Locate every blood parasite and identify its species.
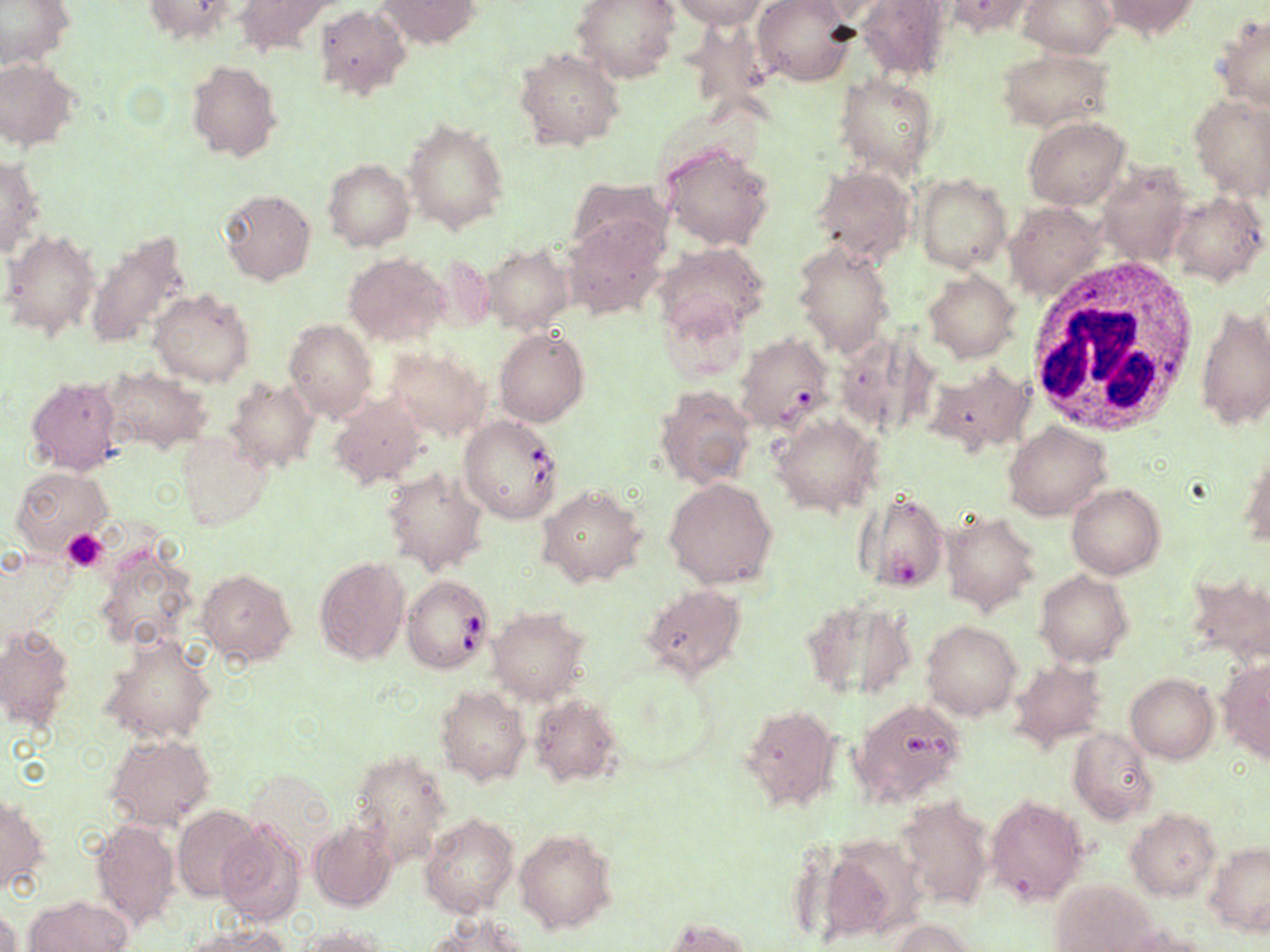

Approximate bounding boxes as (x1, y1, x2, y2) in pixels.
Babesia divergens-infected red blood cells: (733, 339, 831, 431), (459, 415, 564, 523), (403, 575, 494, 675).
No Plasmodium falciparum, Plasmodium ovale, Plasmodium malariae, Plasmodium vivax, or Trypanosoma brucei observed.

Platelet locations: (60, 528, 109, 574). Uninfected red blood cell locations: (0, 0, 73, 67), (142, 0, 240, 45), (232, 0, 340, 54), (376, 0, 479, 48), (572, 0, 681, 83), (671, 0, 770, 28), (755, 0, 858, 87), (1018, 0, 1116, 58), (856, 1, 952, 82), (940, 1, 1044, 39), (1100, 1, 1200, 40), (314, 4, 410, 100), (1217, 14, 1270, 110), (516, 49, 623, 150), (996, 49, 1114, 130), (0, 58, 81, 150), (186, 59, 280, 162), (835, 72, 939, 180), (1190, 93, 1270, 199), (1024, 116, 1129, 209), (403, 118, 508, 234), (659, 142, 776, 251), (0, 154, 44, 260), (323, 158, 415, 251), (1099, 164, 1192, 267), (812, 165, 916, 265), (914, 174, 1011, 273), (566, 177, 672, 257), (219, 189, 316, 286), (1167, 190, 1267, 285), (1005, 202, 1105, 299), (561, 217, 667, 319), (84, 228, 194, 349), (3, 229, 101, 338), (654, 242, 771, 339), (792, 242, 895, 356), (484, 245, 573, 333), (345, 253, 447, 344), (429, 254, 495, 332), (924, 269, 1020, 361), (150, 288, 254, 387), (656, 296, 752, 386), (1196, 303, 1269, 432), (283, 319, 377, 422), (484, 325, 581, 518), (496, 329, 589, 426), (385, 346, 490, 441), (926, 364, 1033, 457), (100, 367, 212, 454), (25, 376, 123, 475), (226, 376, 318, 472), (656, 384, 756, 489), (330, 392, 428, 490), (773, 415, 879, 515), (1003, 422, 1111, 519), (175, 431, 269, 530), (1240, 448, 1269, 547), (11, 466, 112, 553), (383, 467, 485, 575), (664, 477, 778, 590), (1067, 485, 1164, 579), (539, 486, 646, 586), (855, 491, 944, 595), (941, 511, 1041, 615), (92, 541, 201, 656), (313, 555, 409, 666), (197, 568, 296, 664), (1189, 569, 1270, 664), (1036, 571, 1133, 666), (640, 586, 745, 681), (803, 595, 914, 701), (488, 608, 588, 704), (923, 621, 1021, 719), (0, 623, 76, 732), (100, 637, 217, 745), (1009, 658, 1109, 749), (1221, 659, 1270, 761), (1127, 674, 1217, 763), (436, 686, 529, 786), (528, 693, 623, 787), (737, 705, 841, 811), (849, 708, 969, 805), (1068, 727, 1159, 823), (106, 733, 215, 832), (347, 748, 452, 864), (987, 794, 1088, 905), (1, 796, 45, 896), (896, 796, 993, 908), (174, 806, 260, 901), (1127, 808, 1219, 900), (420, 813, 519, 918), (215, 817, 306, 926), (92, 819, 180, 931), (309, 820, 398, 911), (514, 829, 618, 933), (819, 834, 925, 943), (1205, 842, 1269, 936), (1049, 882, 1153, 951), (28, 895, 130, 951), (0, 907, 20, 952), (424, 915, 533, 952), (661, 917, 751, 952), (889, 918, 979, 952), (185, 923, 293, 952), (297, 924, 394, 951), (1115, 926, 1218, 952). White blood cell locations: (1021, 256, 1203, 438). Slide-level diagnosis: Babesia divergens. Image is 1270×952 pixels. Thin blood film. Captured at 1000x magnification. Light microscopy. Single field of view. May-Grünwald-Giemsa-stained preparation.